Name the blood parasite species.
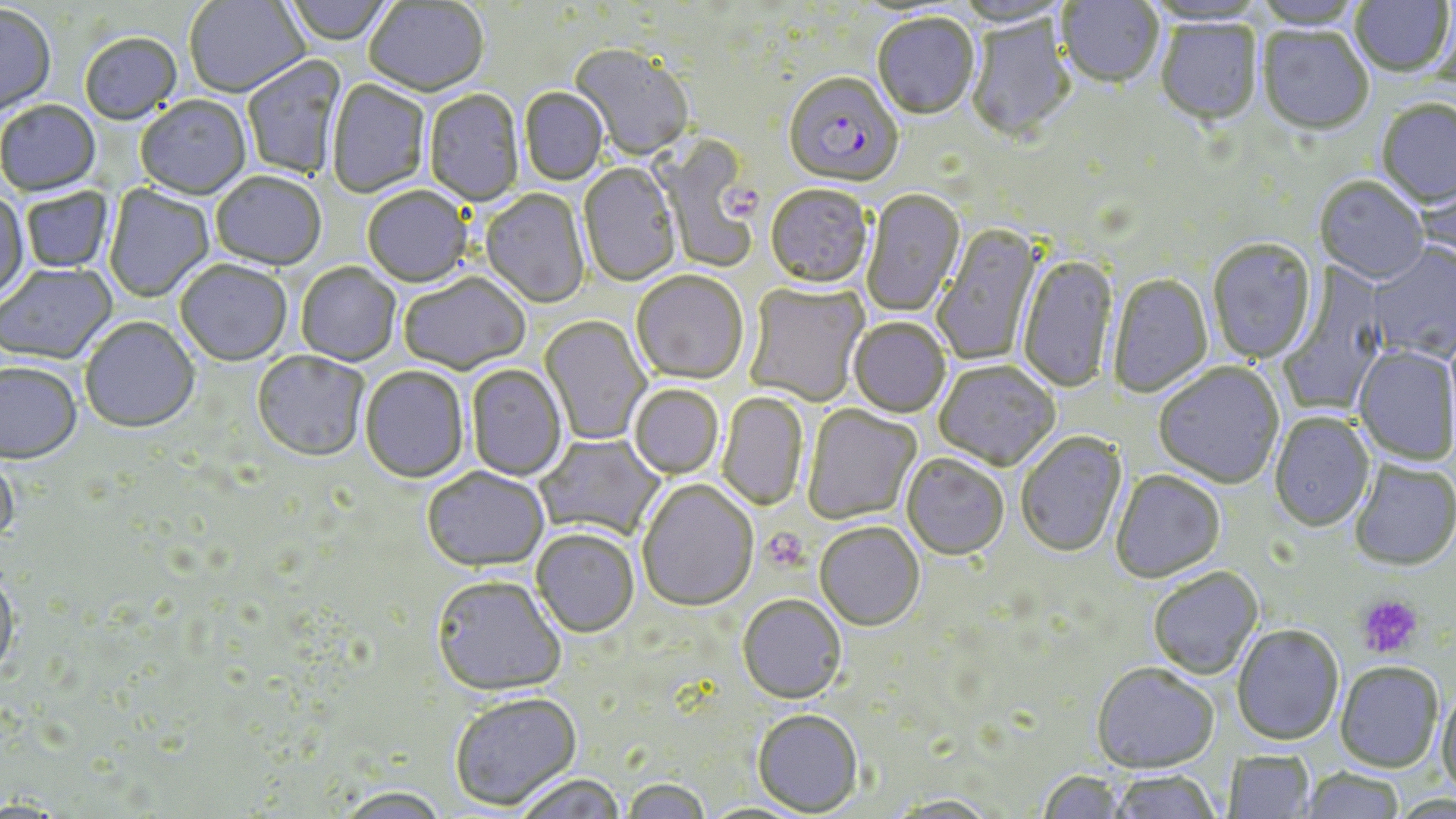
Plasmodium falciparum.

Summary:
  - Coordinate format: approximate bounding boxes as named x1/y1/x2/y2 corners in pixels
  - Plasmodium falciparum-infected red blood cell locations: (x1=783, y1=75, x2=903, y2=191)
  - Platelet locations: (x1=719, y1=184, x2=764, y2=221), (x1=760, y1=527, x2=810, y2=573), (x1=1356, y1=593, x2=1423, y2=657)
  - Uninfected red blood cell locations: (x1=185, y1=0, x2=310, y2=99), (x1=282, y1=0, x2=397, y2=47), (x1=1349, y1=0, x2=1454, y2=78), (x1=952, y1=1, x2=1069, y2=28), (x1=1056, y1=1, x2=1165, y2=91), (x1=365, y1=2, x2=489, y2=98), (x1=0, y1=5, x2=57, y2=118), (x1=872, y1=14, x2=979, y2=122), (x1=964, y1=14, x2=1077, y2=145), (x1=1155, y1=20, x2=1263, y2=129), (x1=1257, y1=27, x2=1374, y2=137), (x1=79, y1=34, x2=183, y2=126), (x1=568, y1=44, x2=695, y2=163), (x1=242, y1=56, x2=347, y2=178), (x1=327, y1=80, x2=431, y2=199), (x1=519, y1=88, x2=609, y2=187), (x1=424, y1=90, x2=523, y2=207), (x1=135, y1=97, x2=251, y2=201), (x1=1376, y1=101, x2=1456, y2=211), (x1=0, y1=102, x2=101, y2=198), (x1=652, y1=135, x2=760, y2=272), (x1=578, y1=164, x2=682, y2=287), (x1=1416, y1=170, x2=1456, y2=270), (x1=210, y1=173, x2=326, y2=272), (x1=1314, y1=178, x2=1429, y2=286), (x1=104, y1=184, x2=215, y2=303), (x1=765, y1=186, x2=873, y2=292), (x1=20, y1=187, x2=115, y2=274), (x1=362, y1=188, x2=472, y2=289), (x1=0, y1=190, x2=29, y2=304), (x1=861, y1=190, x2=966, y2=317), (x1=480, y1=191, x2=590, y2=309), (x1=932, y1=224, x2=1045, y2=366), (x1=1207, y1=240, x2=1317, y2=364), (x1=1368, y1=243, x2=1456, y2=362), (x1=1018, y1=253, x2=1118, y2=395), (x1=175, y1=262, x2=292, y2=367), (x1=0, y1=264, x2=118, y2=366), (x1=296, y1=264, x2=401, y2=367), (x1=1278, y1=264, x2=1391, y2=416), (x1=631, y1=272, x2=749, y2=386), (x1=1108, y1=274, x2=1213, y2=398), (x1=399, y1=275, x2=531, y2=376), (x1=744, y1=283, x2=869, y2=407), (x1=540, y1=315, x2=651, y2=445), (x1=80, y1=318, x2=200, y2=435), (x1=848, y1=319, x2=951, y2=418), (x1=1353, y1=346, x2=1455, y2=466), (x1=251, y1=351, x2=369, y2=465), (x1=933, y1=361, x2=1060, y2=472), (x1=1154, y1=363, x2=1284, y2=490), (x1=0, y1=364, x2=83, y2=467), (x1=465, y1=365, x2=568, y2=481), (x1=359, y1=367, x2=469, y2=484), (x1=628, y1=385, x2=723, y2=480), (x1=717, y1=392, x2=808, y2=512), (x1=802, y1=405, x2=922, y2=525), (x1=1269, y1=412, x2=1375, y2=534), (x1=1015, y1=433, x2=1128, y2=559), (x1=534, y1=434, x2=666, y2=542), (x1=0, y1=451, x2=19, y2=551), (x1=901, y1=455, x2=1010, y2=562), (x1=1350, y1=462, x2=1455, y2=573), (x1=422, y1=469, x2=550, y2=575), (x1=1110, y1=471, x2=1226, y2=584), (x1=637, y1=481, x2=758, y2=613), (x1=814, y1=524, x2=925, y2=633), (x1=531, y1=530, x2=639, y2=639), (x1=1147, y1=568, x2=1263, y2=680), (x1=0, y1=570, x2=20, y2=679), (x1=431, y1=578, x2=566, y2=698), (x1=737, y1=597, x2=846, y2=706), (x1=1231, y1=625, x2=1344, y2=745), (x1=1334, y1=662, x2=1443, y2=772), (x1=1091, y1=664, x2=1219, y2=775), (x1=1436, y1=686, x2=1456, y2=799), (x1=449, y1=694, x2=582, y2=812), (x1=751, y1=711, x2=863, y2=817), (x1=1223, y1=750, x2=1315, y2=818), (x1=1299, y1=768, x2=1404, y2=818), (x1=1036, y1=770, x2=1131, y2=819), (x1=1108, y1=770, x2=1221, y2=819), (x1=514, y1=776, x2=626, y2=818), (x1=620, y1=780, x2=712, y2=819), (x1=336, y1=789, x2=450, y2=819), (x1=887, y1=796, x2=1000, y2=818)
  - Stain: May-Grünwald-Giemsa
  - Preparation: thin blood smear
  - Field of view: single
  - Modality: light microscopy
  - Magnification: 1000x
  - Image size: 1456×819 pixels